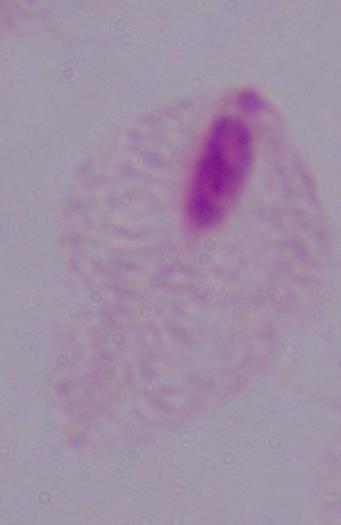
Summary:
  - Identification: trichomonad
  - Modality: photomicrograph
  - Magnification: 1000x